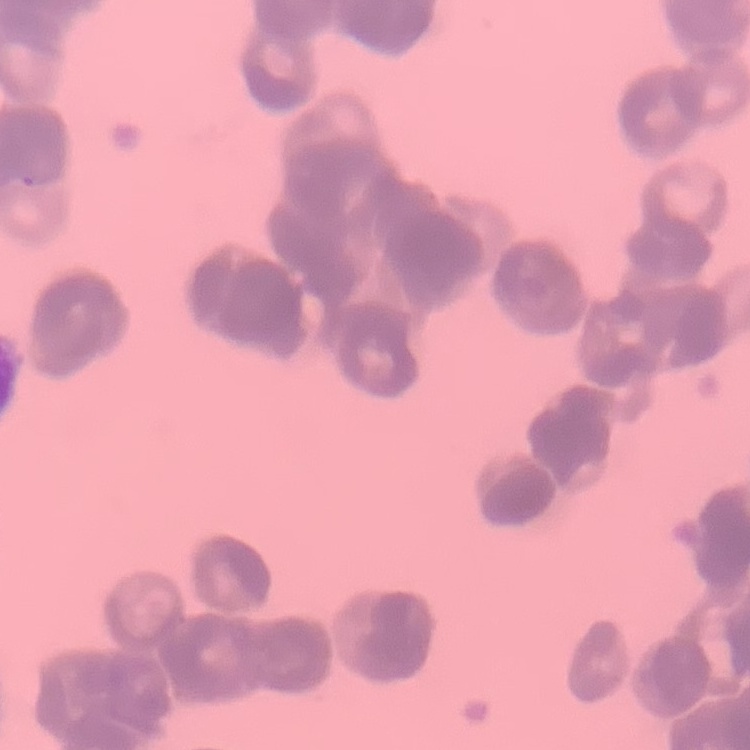

The red blood cells show rouleaux formation. Square crop of a larger photomicrograph. Field's or Giemsa stain. Thin blood smear.